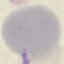
Summary:
  - Malaria status: uninfected
  - Stain: Giemsa
  - Capture: smartphone through the microscope eyepiece
  - Preparation: thin blood film
  - Image type: cell patch, automatically extracted from a larger field of view and resized to 64 × 64 pixels